State the preparation type.
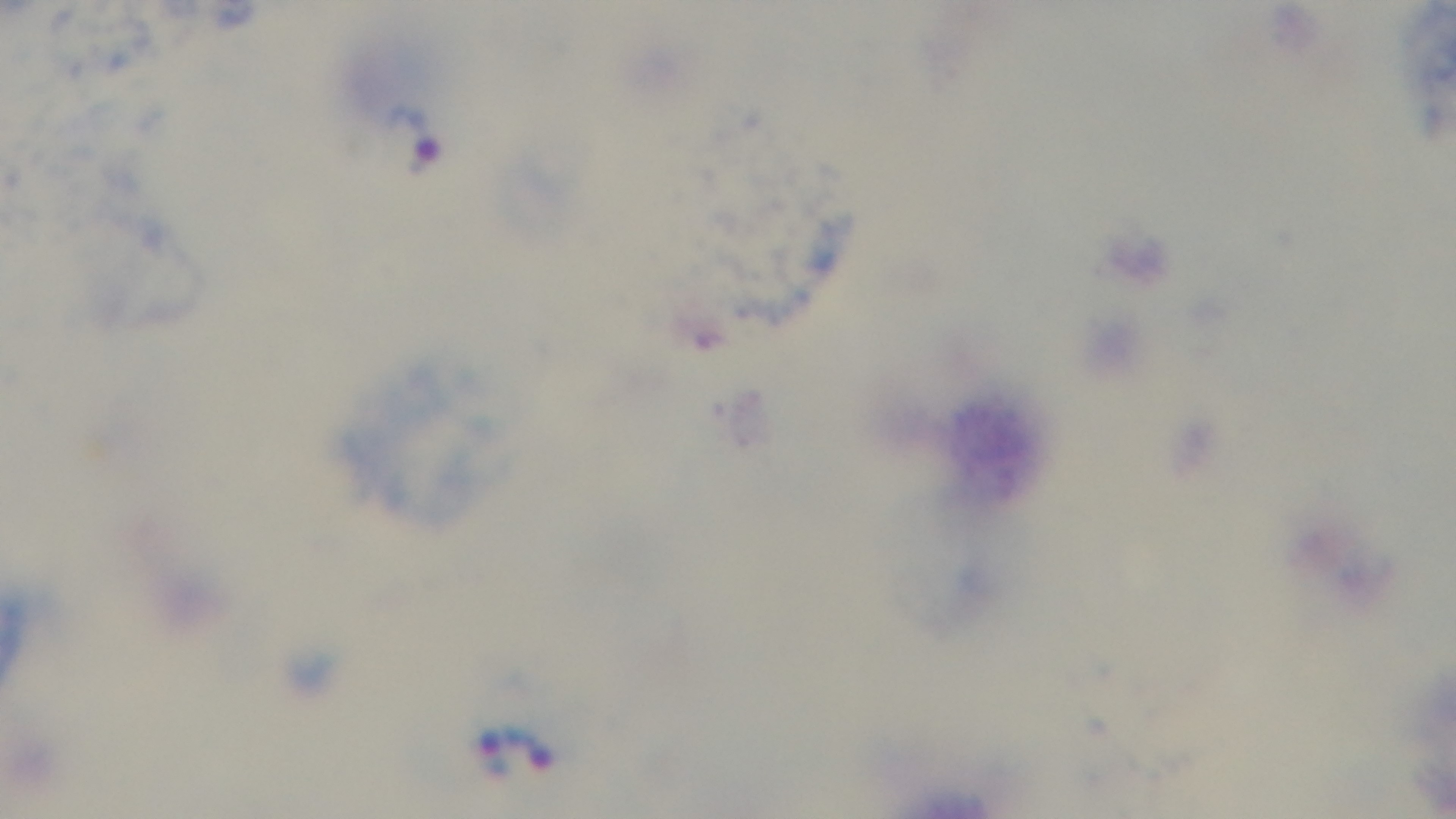

A thick smear.

Malaria status: infected. Giemsa stain. Captured with a mounted 4K digital camera. Photomicrograph. 100x oil-immersion objective. One field from the slide.